Identify the parasite.
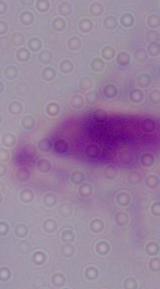

This is a trichomonad.

Micrograph. Captured at 1000x magnification.